Name the parasite shown.
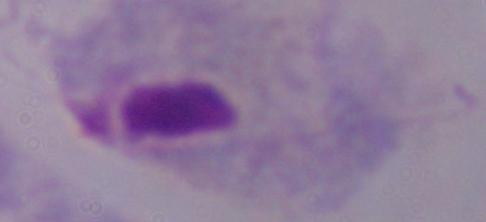

A trichomonad.

magnification = 1000x
modality = micrograph